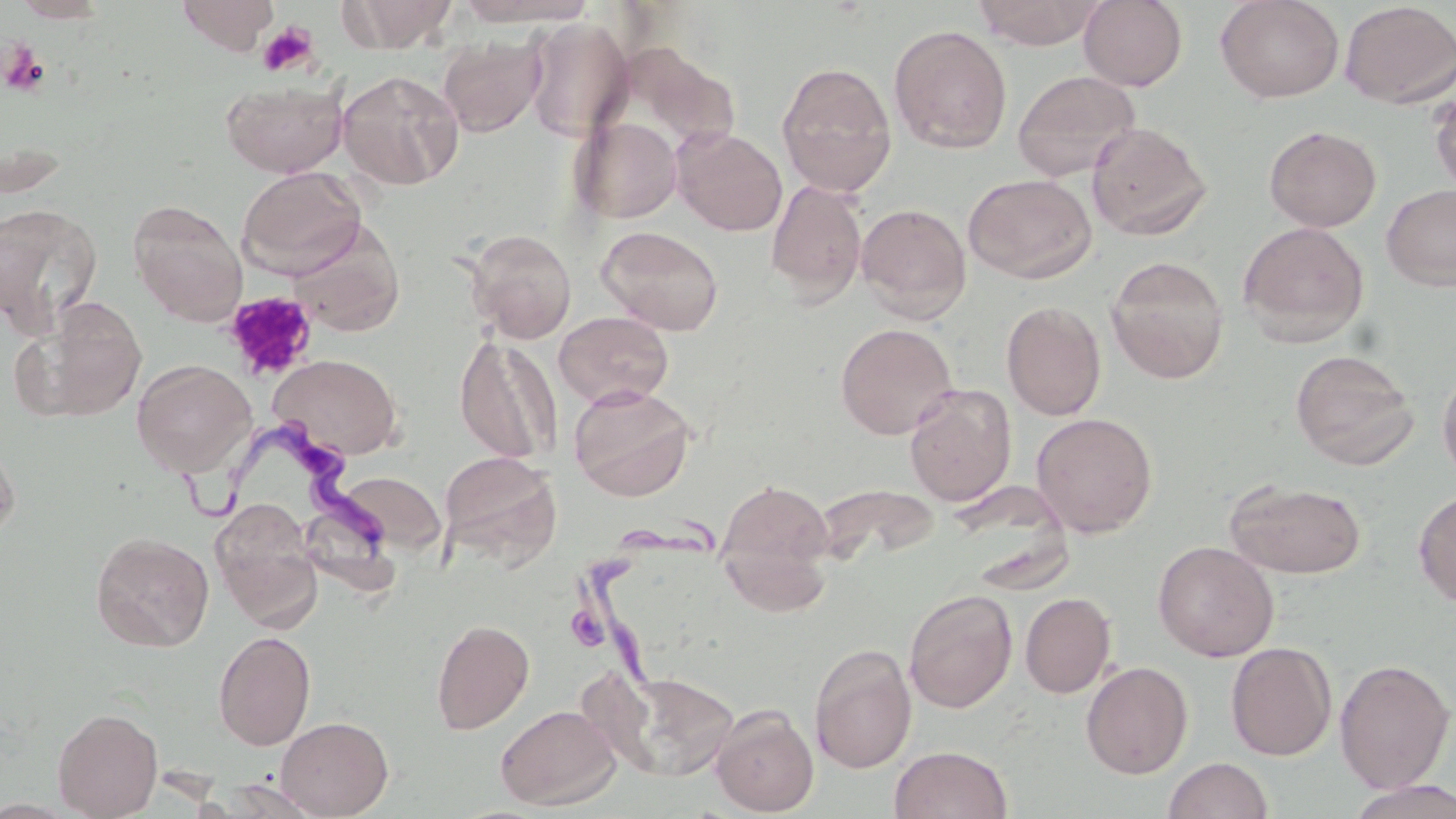
Summary:
  - Coordinate format: approximate bounding boxes as [x1, y1, x2, y2] in pixels
  - Uninfected red blood cell locations: [10, 0, 114, 24], [177, 0, 278, 54], [341, 0, 458, 53], [453, 0, 596, 27], [972, 0, 1106, 49], [1078, 0, 1188, 91], [1215, 0, 1344, 103], [1339, 1, 1456, 109], [523, 18, 634, 142], [889, 24, 1013, 154], [438, 34, 546, 137], [776, 61, 897, 197], [336, 70, 464, 190], [1012, 70, 1140, 182], [220, 78, 348, 177], [1430, 86, 1456, 195], [571, 116, 682, 224], [1086, 122, 1212, 240], [1263, 125, 1382, 232], [673, 127, 787, 236], [237, 166, 366, 277], [963, 173, 1097, 284], [766, 180, 867, 305], [1381, 183, 1456, 291], [128, 199, 248, 325], [0, 203, 103, 332], [856, 203, 972, 321], [288, 221, 405, 336], [1238, 221, 1370, 345], [596, 225, 724, 336], [466, 229, 577, 343], [1105, 256, 1230, 383], [12, 295, 148, 423], [1001, 301, 1106, 421], [554, 311, 673, 409], [835, 322, 958, 439], [455, 334, 560, 463], [1290, 349, 1419, 469], [269, 353, 403, 459], [132, 358, 256, 477], [1437, 366, 1456, 485], [568, 384, 696, 502], [904, 384, 1016, 506], [1030, 412, 1157, 538], [0, 435, 20, 544], [439, 451, 561, 567], [335, 471, 446, 554], [716, 478, 835, 610], [1224, 480, 1368, 578], [1413, 488, 1456, 608], [213, 504, 324, 632], [90, 532, 214, 652], [1153, 540, 1279, 662], [904, 588, 1018, 713], [1020, 592, 1116, 698], [431, 618, 534, 734], [213, 631, 316, 750], [1226, 642, 1337, 761], [808, 643, 917, 773], [1334, 658, 1454, 793], [1080, 661, 1193, 779], [601, 670, 740, 782], [495, 704, 620, 810], [710, 704, 819, 816], [52, 707, 163, 818], [275, 716, 394, 818], [889, 745, 1013, 819], [1162, 757, 1275, 819], [220, 778, 325, 818], [1343, 779, 1456, 819]
  - Trypanosoma brucei locations: [181, 432, 401, 562], [571, 514, 721, 698]
  - Platelet locations: [257, 21, 319, 77], [1, 41, 50, 97], [223, 290, 318, 382]
  - Slide-level diagnosis: Trypanosoma brucei
  - Field of view: single
  - Magnification: 1000x
  - Modality: light microscopy
  - Preparation: thin blood smear
  - Stain: May-Grünwald-Giemsa
  - Image size: 1456×819 pixels